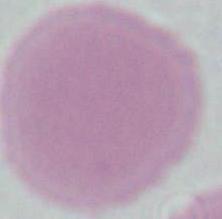
modality = photomicrograph
identification = erythrocyte
magnification = 1000x